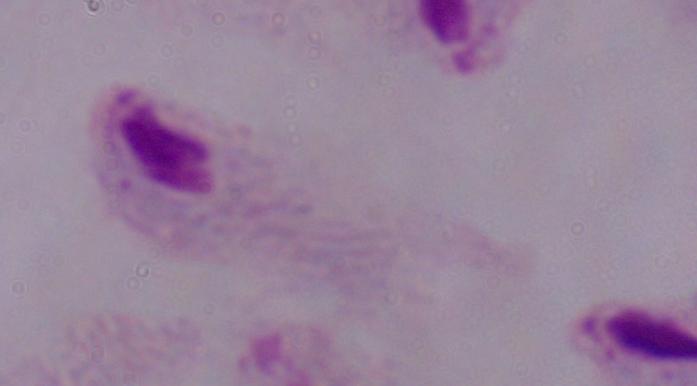
magnification = 1000x
modality = photomicrograph
identification = trichomonad